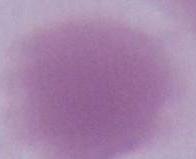

An erythrocyte is seen. Photomicrograph. 1000x magnification.